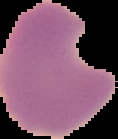
image type = segmented cell region with the area outside set to black
result = Plasmodium parasites identified
preparation = thin blood smear
image size = 118×139 pixels